Draw a bounding box around every parasitised red blood cell.
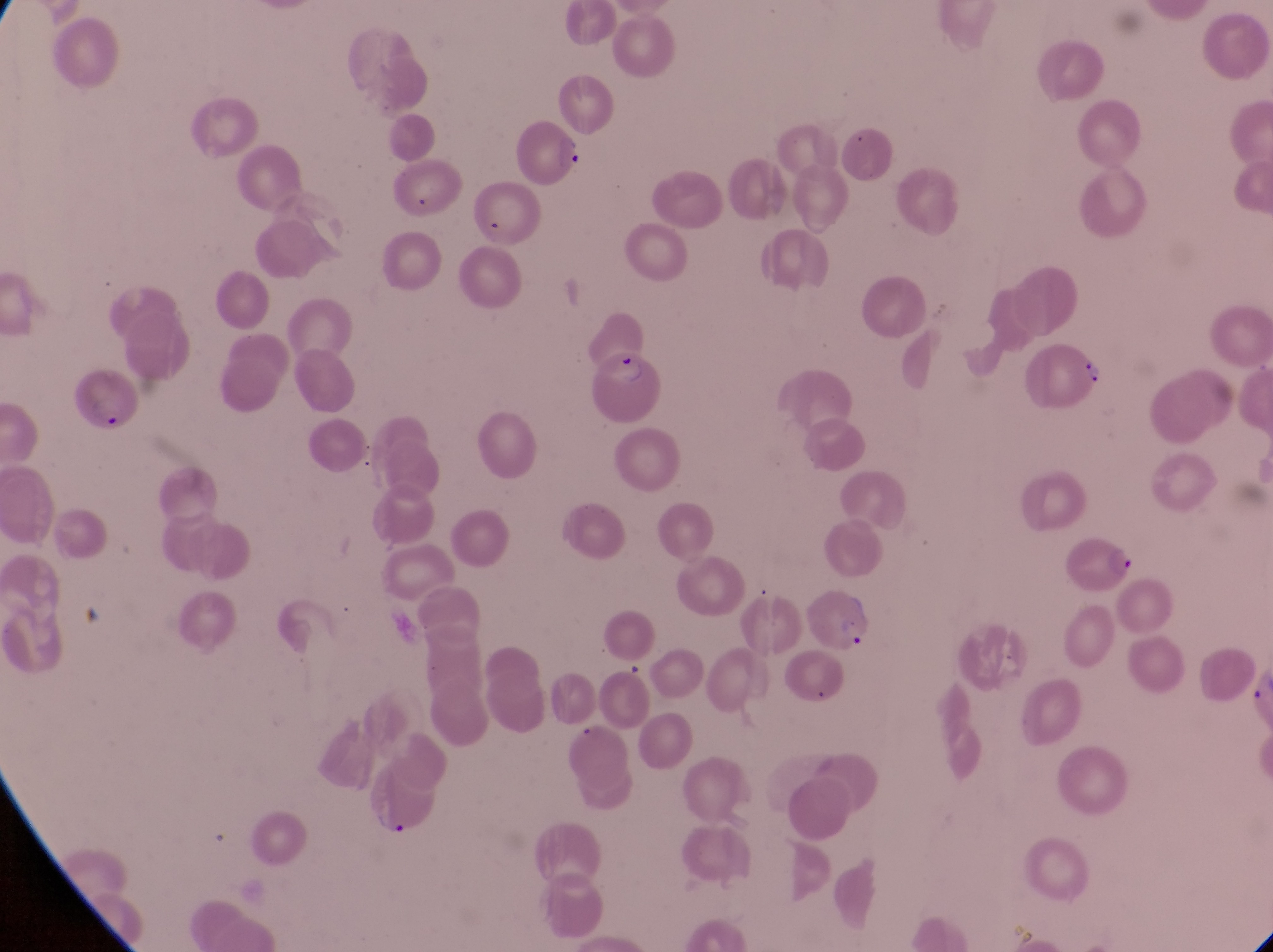
Approximate bounding boxes as left top right bottom in pixels.
Parasitised red blood cells: 514 122 591 190; 1029 337 1111 420; 597 345 666 428; 65 370 147 440; 1069 535 1139 597; 808 586 883 666; 374 764 449 842.

{
  "capture": "smartphone photograph through the eyepiece of an Olympus CX-23 microscope",
  "country": "Uganda",
  "preparation": "thin blood smear",
  "magnification": "1000x",
  "field_of_view": "single",
  "image_size": "1273×952 pixels"
}